Locate and identify every blood parasite.
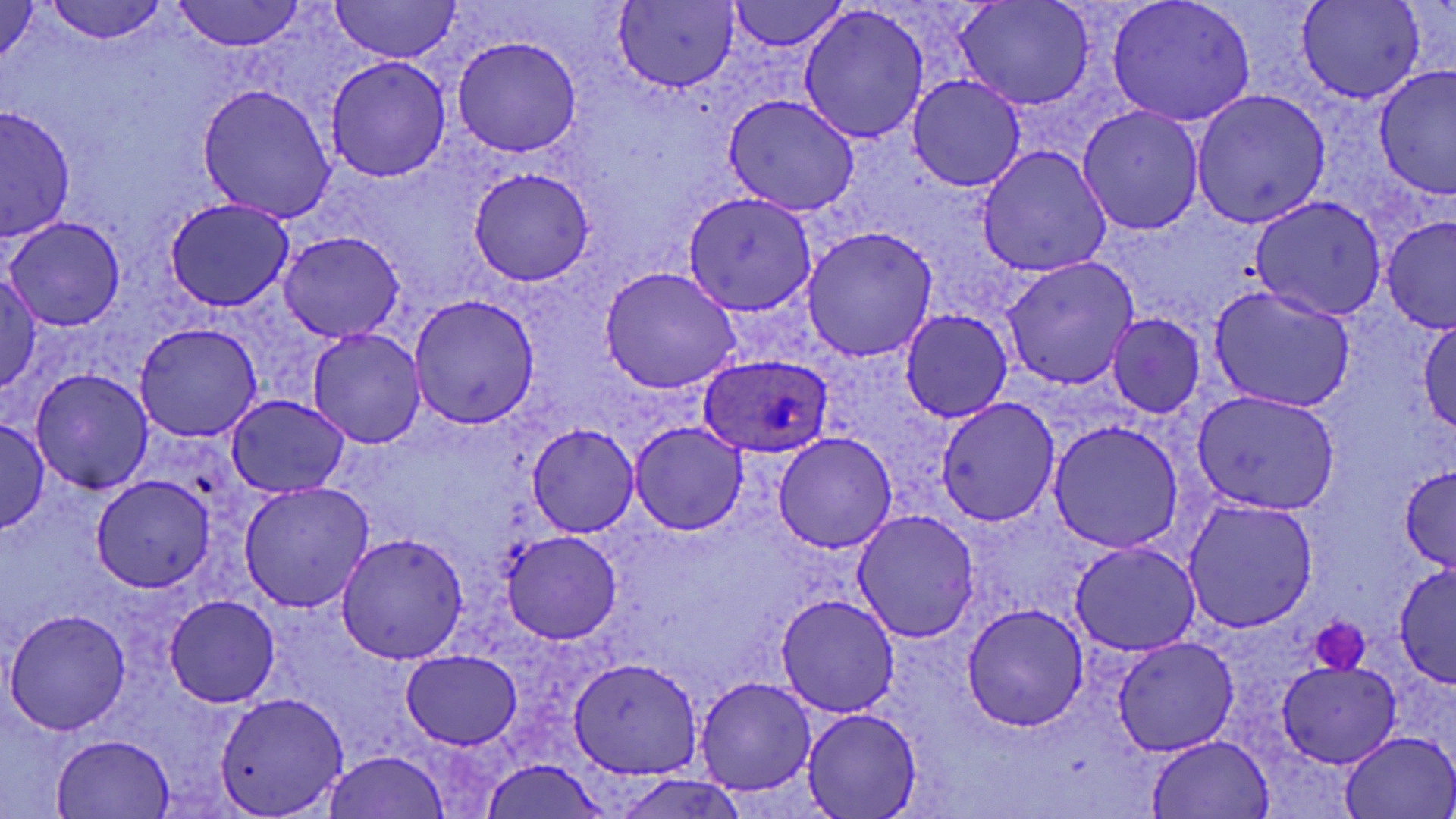

Approximate bounding boxes as (x1,y1)-(x2,y2) corner pairs in pixels.
Plasmodium ovale-infected red blood cells: (698,354)-(832,458).
No Plasmodium falciparum, Plasmodium malariae, Plasmodium vivax, Babesia divergens, or Trypanosoma brucei observed.

Uninfected red blood cell locations: (44,0)-(168,43), (173,0)-(304,53), (328,0)-(466,64), (728,0)-(849,54), (955,0)-(1097,111), (1105,0)-(1258,129), (1295,0)-(1427,103), (615,1)-(740,91), (0,2)-(44,67), (797,4)-(930,143), (451,35)-(587,157), (324,57)-(450,183), (1374,68)-(1453,200), (906,73)-(1026,192), (194,82)-(339,223), (1189,89)-(1331,227), (721,95)-(862,217), (1077,104)-(1206,236), (1,107)-(78,242), (976,144)-(1111,277), (465,168)-(594,286), (681,189)-(819,316), (1249,195)-(1390,321), (163,197)-(294,312), (1381,215)-(1456,337), (6,216)-(125,330), (798,224)-(940,363), (278,232)-(405,342), (1000,256)-(1140,390), (598,264)-(742,396), (0,268)-(51,398), (1208,283)-(1359,413), (407,292)-(539,431), (898,306)-(1014,423), (1412,312)-(1456,444), (1103,313)-(1208,419), (133,321)-(264,442), (305,326)-(427,450), (28,367)-(157,495), (1190,390)-(1341,516), (226,394)-(351,497), (936,396)-(1060,528), (1045,419)-(1186,556), (0,420)-(49,534), (629,420)-(748,534), (525,426)-(640,536), (771,431)-(899,553), (1400,464)-(1456,573), (89,474)-(219,593), (238,481)-(375,612), (1180,495)-(1320,635), (850,510)-(982,644), (501,530)-(621,643), (334,531)-(471,665), (1069,539)-(1205,656), (1395,563)-(1455,681), (774,594)-(902,717), (164,595)-(279,709), (961,601)-(1091,733), (5,607)-(131,736), (1108,633)-(1240,756), (399,650)-(520,749), (569,657)-(701,781), (1277,658)-(1400,768), (695,676)-(818,797), (213,689)-(348,817), (799,708)-(923,819), (1338,729)-(1455,819), (53,734)-(175,817), (1147,734)-(1273,817), (320,750)-(450,819), (477,760)-(609,819). Platelet locations: (1311,613)-(1371,674). Slide-level diagnosis: Plasmodium ovale. Image is 1456×819 pixels. Thin blood smear. Light microscopy. May-Grünwald-Giemsa-stained preparation. One field of a larger specimen. Captured at 1000x magnification.